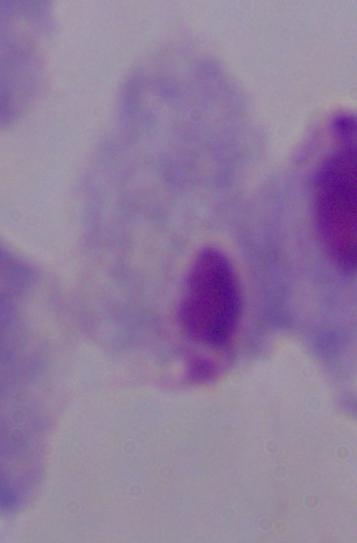
Summary:
  - Modality: micrograph
  - Identification: trichomonad
  - Magnification: 1000x